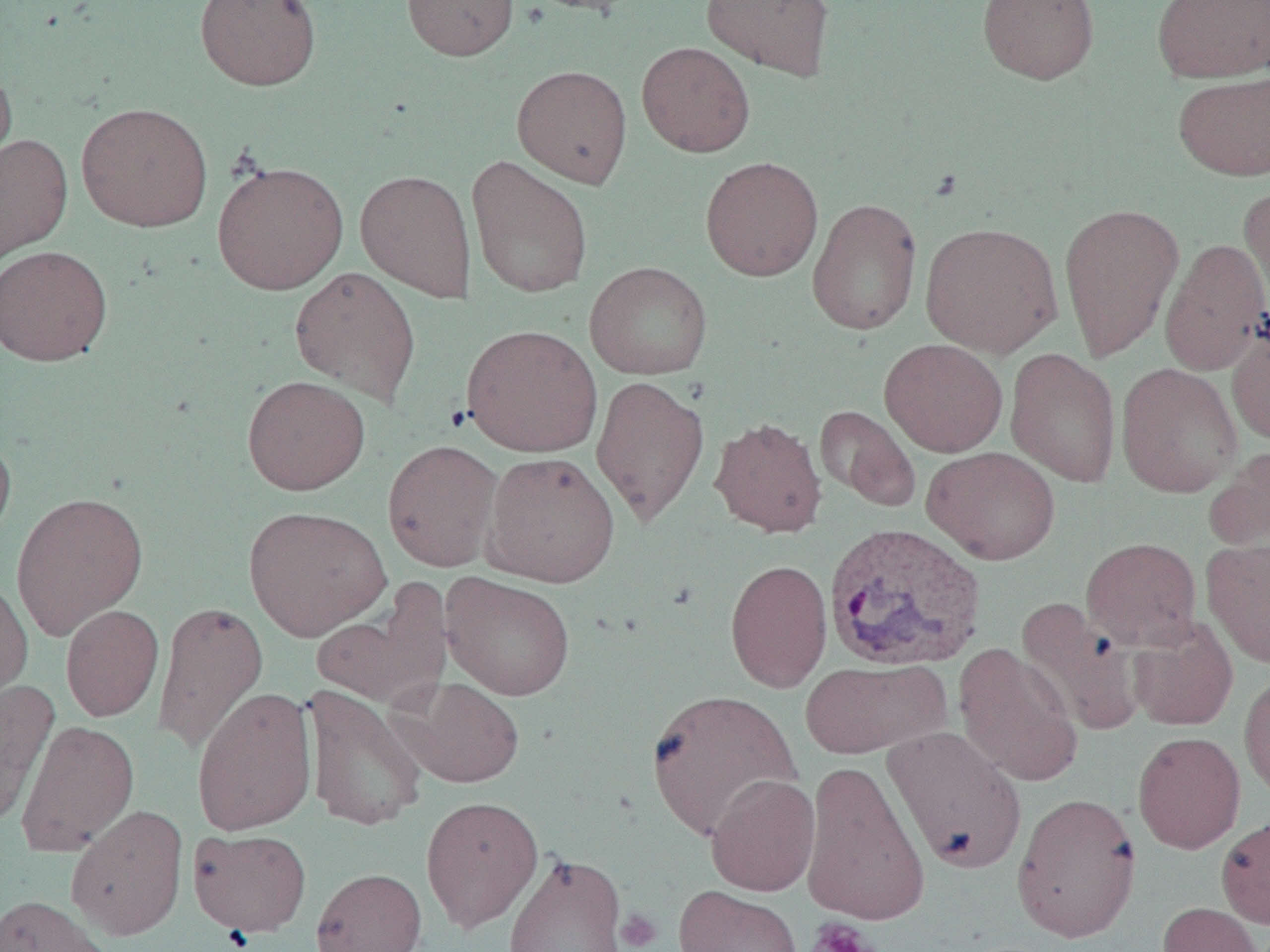

Plasmodium vivax-infected red blood cell locations = approximate bounding boxes as (x1,y1)-(x2,y2) corner pairs in pixels: (823,522)-(986,673)
slide-level diagnosis = Plasmodium vivax
preparation = thin blood smear
field of view = single
platelet locations = approximate bounding boxes as (x1,y1)-(x2,y2) corner pairs in pixels: (615,909)-(662,951), (806,918)-(878,952)
image size = 1270×952 pixels
magnification = 1000x
uninfected red blood cell locations = approximate bounding boxes as (x1,y1)-(x2,y2) corner pairs in pixels: (194,0)-(322,91), (401,0)-(519,61), (517,0)-(643,15), (701,0)-(835,82), (977,0)-(1099,84), (1151,0)-(1270,83), (636,42)-(755,156), (0,60)-(16,179), (511,64)-(633,188), (1172,72)-(1270,181), (76,102)-(214,232), (0,133)-(73,266), (465,154)-(593,299), (700,156)-(823,281), (211,160)-(349,295), (355,169)-(476,302), (1238,182)-(1270,318), (807,197)-(923,335), (1059,202)-(1185,363), (920,221)-(1063,358), (1160,238)-(1270,376), (0,244)-(113,366), (583,261)-(713,380), (289,266)-(422,405), (1226,318)-(1270,448), (461,324)-(602,457), (879,338)-(1008,458), (1005,347)-(1121,487), (1115,363)-(1243,497), (591,373)-(710,527), (241,375)-(371,495), (814,405)-(919,510), (709,416)-(827,538), (0,428)-(17,550), (382,439)-(503,571), (1205,445)-(1270,554), (922,446)-(1061,565), (482,451)-(620,588), (11,491)-(148,640), (243,506)-(391,640), (1081,536)-(1202,651), (1201,539)-(1270,668), (725,558)-(832,692), (439,572)-(576,701), (0,575)-(33,710), (311,588)-(450,712), (1015,598)-(1147,736), (152,601)-(268,755), (60,604)-(164,721), (1128,618)-(1238,731), (953,644)-(1083,789), (799,659)-(951,759), (1239,668)-(1270,801), (398,677)-(524,788), (0,681)-(59,828), (303,684)-(428,832), (191,686)-(317,836), (645,689)-(802,841), (16,719)-(139,856), (883,724)-(1027,873), (1132,732)-(1245,853), (799,759)-(930,927), (705,774)-(820,897), (1011,792)-(1141,942), (420,795)-(543,933), (65,804)-(189,940), (1216,813)-(1270,929), (187,828)-(312,937), (501,850)-(629,951), (311,867)-(428,952), (674,886)-(803,952), (0,894)-(114,952), (1157,901)-(1266,952)
modality = optical microscopy